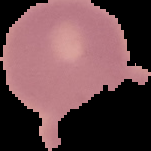
preparation = thin blood smear
image type = cell region segmented out of the field of view; surrounding area masked to black
image size = 151×151 pixels
malaria status = uninfected